Identify the parasite.
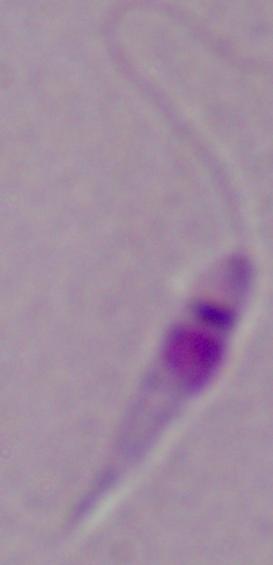

Leishmania.

{
  "modality": "micrograph",
  "magnification": "1000x"
}